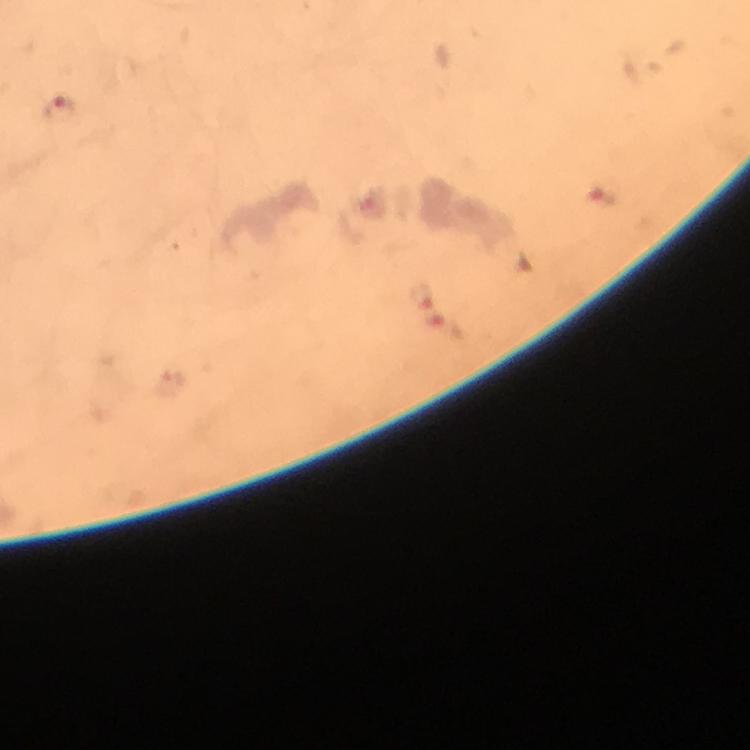
Approximate centers as {x, y} in pixels. Malaria parasite locations: {62, 111}, {601, 198}. Photographed through the microscope with a smartphone camera. From a malaria diagnostic workup. Image is 750×750 pixels. A crop from one field of view. 100x magnification. Thick blood film. Immersion oil was used. Giemsa-stained preparation.